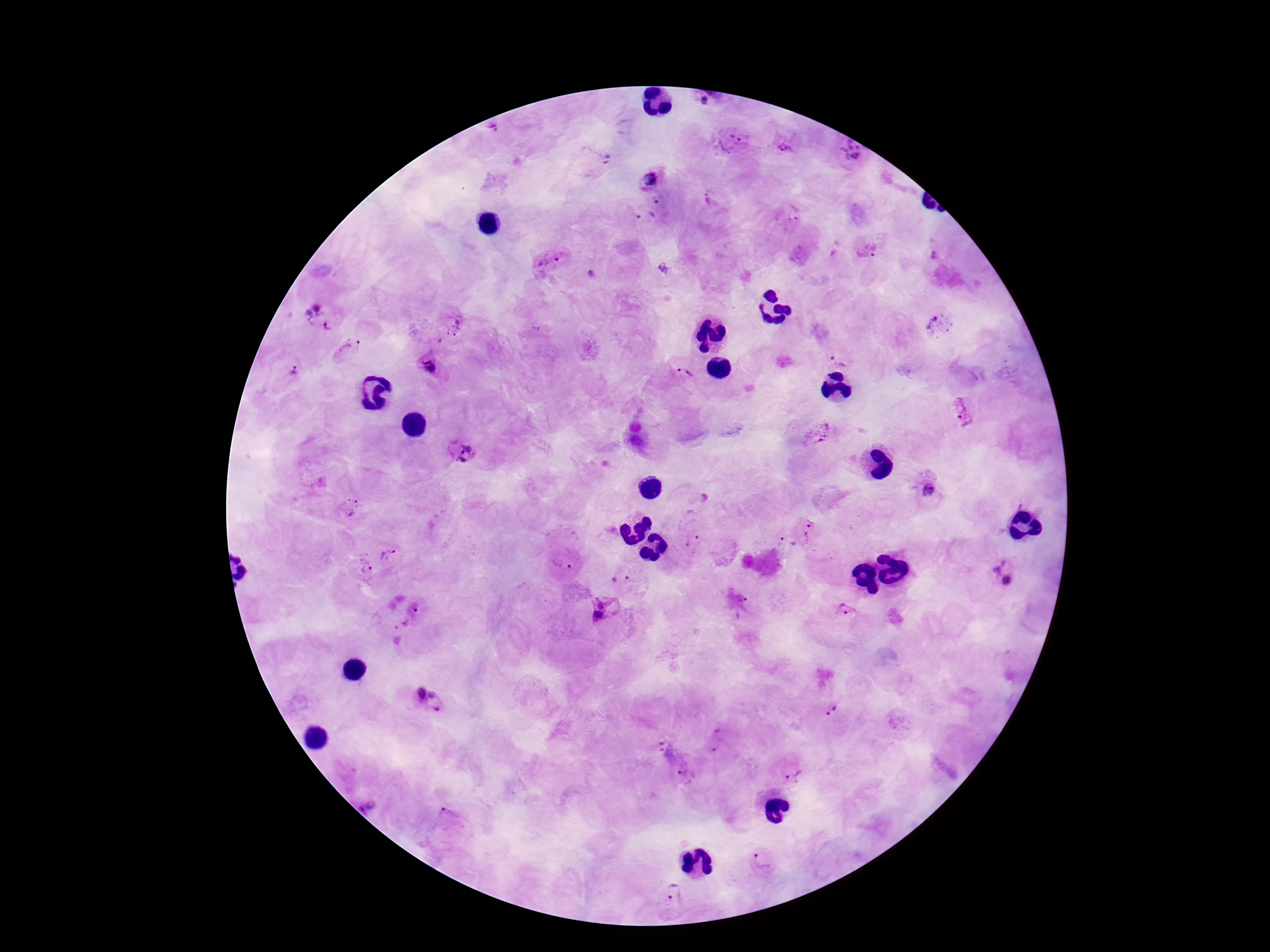
Approximate centers as {x, y} in pixels. Plasmodium parasite locations: {705, 100}, {492, 130}, {732, 140}, {787, 146}, {850, 156}, {599, 163}, {650, 177}, {712, 198}, {661, 203}, {789, 213}, {643, 218}, {869, 247}, {550, 261}, {590, 276}, {320, 315}, {942, 325}, {453, 326}, {346, 349}, {841, 357}, {430, 368}, {291, 371}, {684, 374}, {964, 414}, {817, 433}, {462, 451}, {929, 491}, {349, 507}, {811, 530}, {692, 541}, {787, 544}, {390, 555}, {565, 563}, {362, 566}, {621, 570}, {1002, 572}, {604, 608}, {848, 611}, {429, 701}, {829, 709}, {716, 740}, {666, 751}, {795, 777}, {687, 778}, {449, 822}, {765, 861}, {676, 896}. Thick blood film. Image is 1270×952 pixels. 100x magnification. Photographed through the microscope eyepiece with a smartphone camera. Patient malaria status: infected. Single field of view. Giemsa-stained preparation.